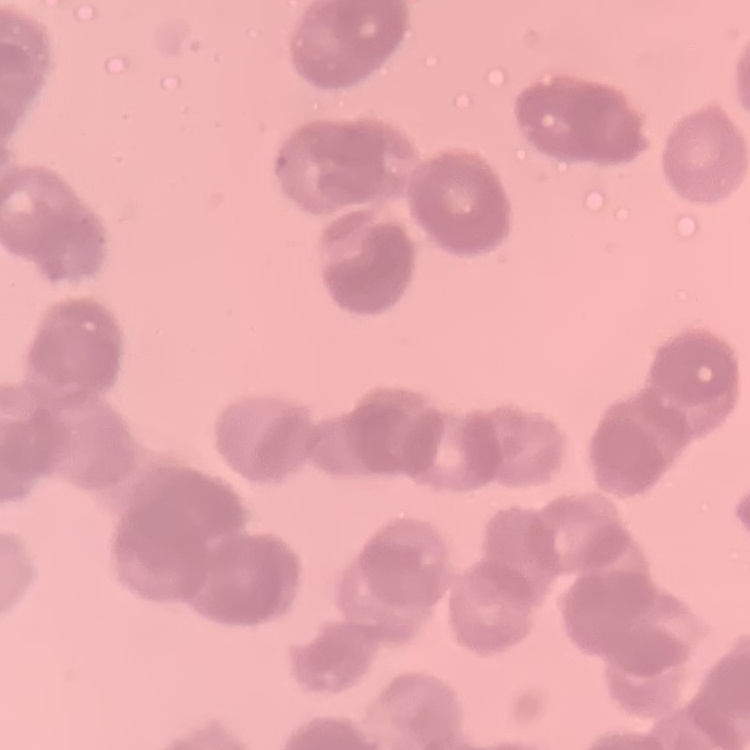
red blood cell morphology = rouleaux formation
stain = Field's or Giemsa
image type = square crop of a larger photomicrograph
preparation = thin peripheral smear